Name the cell type shown.
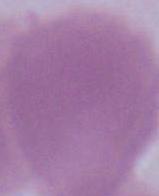

This is an erythrocyte.

Summary:
  - Modality: photomicrograph
  - Magnification: 1000x